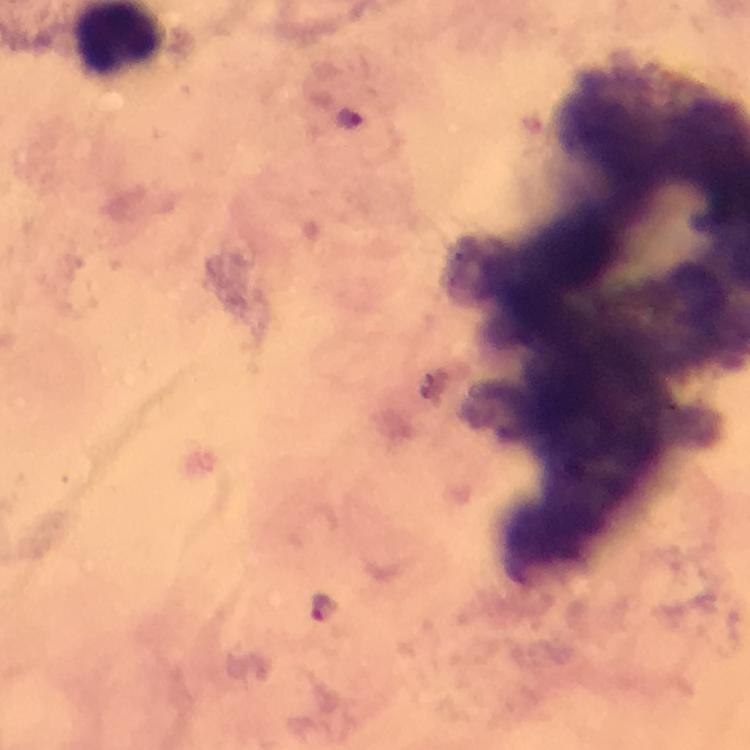
Approximate object centers, in pixels from the top-left corner.
Summary:
  - Malaria parasite locations: (x=348, y=119), (x=325, y=607)
  - Magnification: 100x
  - Stain: Giemsa
  - Context: from a diagnostic examination for malaria
  - Immersion oil: used
  - Image size: 750×750 pixels
  - Capture: smartphone mounted on the microscope
  - Cropped from: one field of view
  - Preparation: thick smear